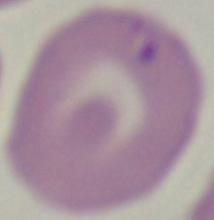

modality: micrograph
magnification: 1000x
identification: Babesia